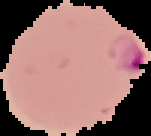
preparation = thin blood film
malaria status = parasitized
image type = segmented cell region with the area outside set to black
image size = 151×136 pixels